Name the cell type shown.
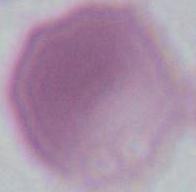
An erythrocyte.

1000x magnification. Photomicrograph.